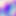

400x magnification. Micrograph. Toxoplasma gondii is shown.